State the preparation type.
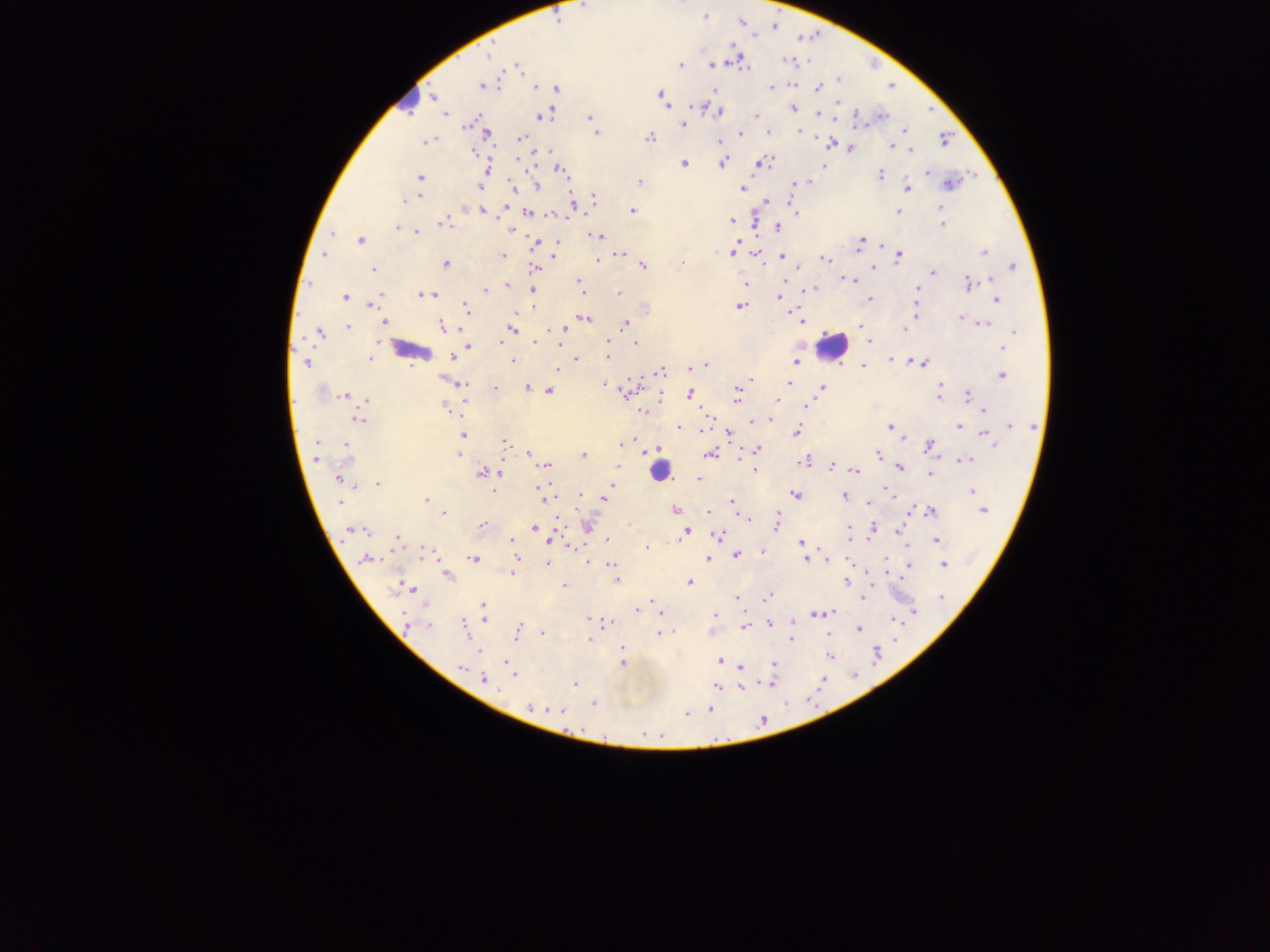

This is a thick smear.

Approximate centers as (x, y) in pixels.
Summary:
  - Plasmodium parasite locations: (583, 6), (704, 17), (741, 22), (774, 26), (488, 54), (787, 61), (680, 64), (711, 65), (517, 66), (838, 80), (482, 86), (535, 87), (771, 87), (818, 88), (556, 89), (714, 91), (661, 95), (432, 97), (664, 101), (839, 102), (793, 108), (719, 113), (819, 113), (445, 115), (546, 115), (756, 115), (882, 115), (590, 117), (467, 125), (684, 125), (798, 130), (768, 132), (597, 133), (740, 134), (487, 136), (521, 136), (649, 137), (945, 139), (720, 141), (425, 142), (830, 143), (893, 145), (851, 148), (546, 150), (910, 150), (473, 152), (722, 163), (762, 163), (684, 164), (487, 169), (560, 170), (928, 173), (880, 175), (419, 177), (639, 181), (808, 182), (511, 184), (950, 184), (795, 185), (480, 186), (537, 186), (908, 188), (742, 189), (418, 197), (410, 199), (595, 200), (403, 201), (767, 201), (573, 203), (505, 207), (466, 208), (481, 210), (632, 210), (898, 211), (796, 212), (528, 213), (551, 214), (732, 221), (442, 223), (942, 224), (398, 227), (778, 228), (510, 229), (416, 231), (332, 233), (598, 236), (360, 240), (861, 241), (534, 243), (556, 244), (984, 252), (733, 253), (621, 254), (323, 255), (555, 255), (503, 256), (781, 256), (899, 256), (602, 257), (597, 259), (825, 259), (447, 264), (682, 264), (643, 266), (874, 267), (1012, 267), (535, 268), (798, 268), (374, 269), (933, 272), (849, 280), (992, 280), (579, 282), (783, 282), (745, 284), (968, 284), (506, 285), (814, 289), (918, 289), (485, 291), (532, 291), (582, 292), (619, 293), (380, 294), (426, 294), (344, 296), (780, 298), (870, 299), (997, 300), (373, 301), (740, 306), (465, 307), (533, 307), (917, 311), (961, 318), (586, 319), (801, 320), (384, 322), (625, 324), (985, 324), (442, 326), (859, 326), (348, 327), (512, 328), (905, 329), (550, 330), (1015, 332), (319, 333), (534, 341), (608, 341), (869, 341), (500, 342), (636, 343), (467, 346), (1003, 348), (607, 356), (453, 357), (369, 358), (575, 359), (512, 361), (892, 361), (796, 362), (306, 363), (923, 363), (705, 364), (863, 366), (694, 367), (557, 369), (661, 372), (1002, 375), (750, 380), (789, 383), (461, 384), (606, 384), (941, 385), (495, 388), (526, 388), (822, 388), (627, 390), (549, 391), (737, 392), (344, 395), (690, 395), (939, 395), (967, 396), (368, 400), (736, 400), (777, 400), (806, 406), (444, 408), (984, 409), (643, 411), (768, 419), (360, 420), (753, 421), (1010, 425), (679, 427), (890, 427), (958, 427), (705, 428), (796, 431), (729, 435), (985, 435), (462, 436), (904, 438), (992, 440), (505, 442), (316, 443), (622, 444), (930, 445), (346, 446), (656, 449), (758, 450), (529, 454), (710, 454), (879, 454), (458, 455), (583, 456), (316, 459), (965, 460), (804, 461), (546, 466), (617, 466), (832, 466), (900, 468), (855, 471), (482, 474), (930, 474), (338, 478), (698, 479), (376, 484), (613, 485), (538, 489), (610, 489), (885, 490), (972, 491), (493, 492), (580, 495), (796, 495), (844, 496), (604, 498), (426, 500), (340, 502), (731, 502), (868, 503), (675, 509), (983, 511), (931, 512), (709, 513), (444, 514), (746, 518), (557, 520), (777, 524), (482, 525), (587, 525), (850, 528), (534, 529), (873, 529), (358, 530), (350, 531), (365, 531), (899, 531), (686, 532), (717, 535), (606, 539), (398, 540), (511, 541), (549, 541), (937, 541), (801, 542), (646, 548), (424, 551), (763, 552), (803, 553), (736, 555), (473, 558), (709, 558), (367, 559), (805, 560), (827, 560), (588, 561), (547, 564), (611, 564), (908, 564), (943, 565), (515, 568), (512, 573), (448, 576), (616, 580), (690, 582), (846, 582), (564, 585), (406, 588), (396, 589), (414, 590), (737, 597), (768, 597), (941, 597), (862, 598), (652, 601), (483, 605), (641, 608), (637, 610), (915, 612), (817, 613), (661, 614), (715, 615), (484, 618), (589, 618), (405, 619), (895, 620), (770, 622), (607, 623), (793, 623), (430, 626), (744, 627), (465, 628), (858, 629), (518, 630), (543, 633), (661, 634), (791, 639), (589, 640), (624, 648), (478, 651), (877, 654), (830, 656), (720, 661), (623, 663), (774, 664), (507, 665), (741, 667), (461, 668), (512, 674), (478, 676), (483, 679), (574, 683), (770, 683), (717, 686), (744, 686), (498, 691), (593, 703), (529, 707), (553, 709), (709, 710), (561, 712), (686, 715)
  - Leukocyte locations: (404, 94), (832, 345), (406, 350), (661, 474)
  - Capture: mobile-phone photograph through a microscope
  - Field of view: single
  - Image size: 1270×952 pixels
  - Country: Ghana